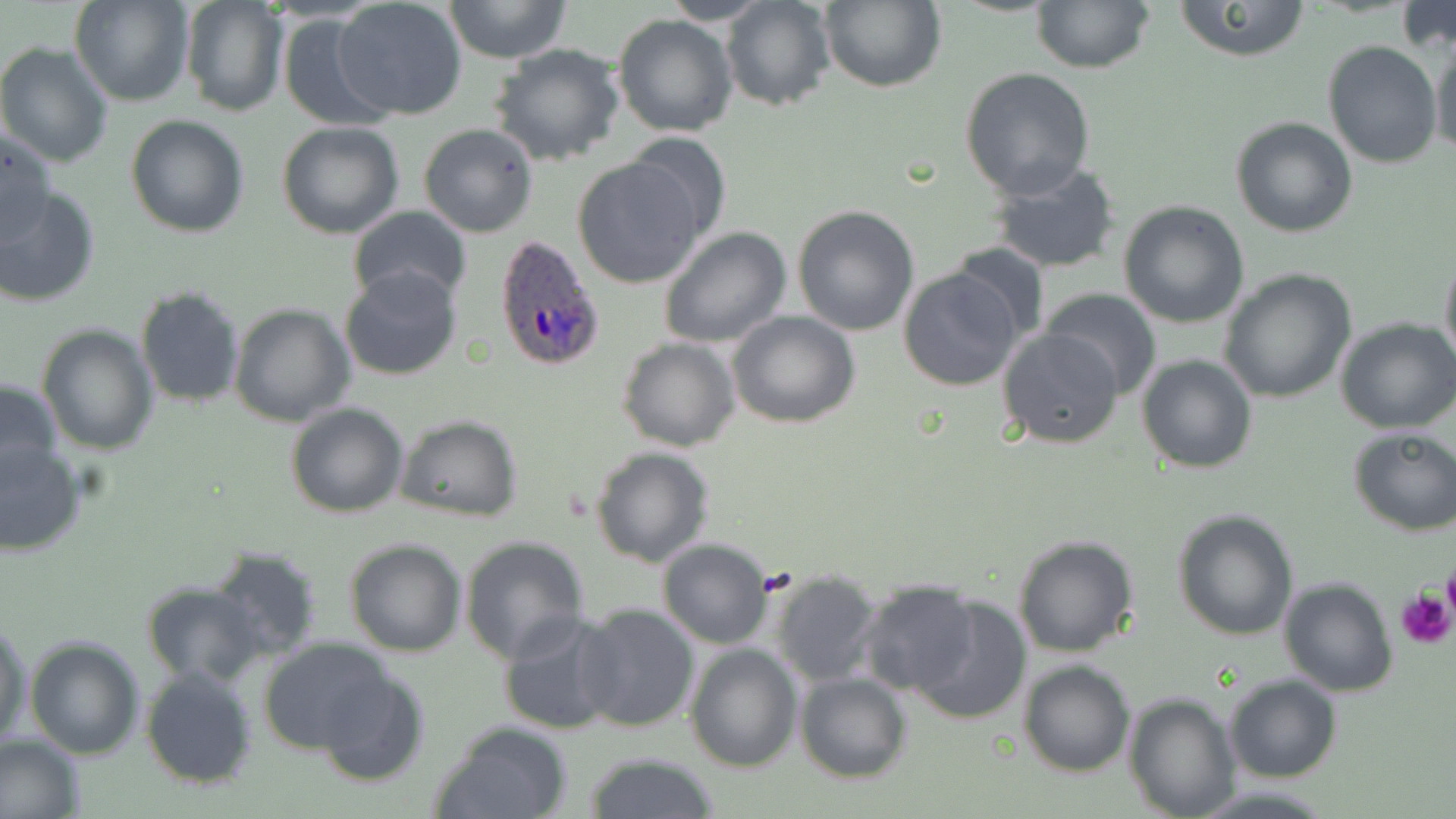
slide-level diagnosis = Plasmodium ovale
modality = optical microscopy
preparation = thin blood smear
uninfected red blood cell locations = approximate bounding boxes as (x1, y1, x2, y2) in pixels: (70, 0, 195, 106), (443, 0, 572, 62), (658, 0, 772, 25), (719, 0, 836, 113), (820, 0, 947, 93), (1172, 0, 1313, 61), (1030, 1, 1155, 72), (179, 2, 288, 117), (332, 2, 468, 122), (1395, 4, 1456, 53), (613, 12, 740, 138), (277, 14, 397, 132), (1428, 36, 1455, 160), (1322, 40, 1442, 169), (0, 42, 117, 169), (489, 43, 628, 168), (959, 65, 1096, 199), (124, 115, 250, 239), (1231, 116, 1359, 238), (277, 122, 404, 239), (419, 122, 540, 239), (2, 125, 55, 247), (620, 131, 733, 244), (572, 156, 708, 289), (987, 160, 1122, 276), (0, 186, 100, 309), (1117, 199, 1250, 328), (792, 203, 922, 336), (347, 205, 473, 310), (658, 226, 791, 349), (947, 240, 1050, 344), (1439, 252, 1456, 375), (340, 266, 461, 381), (897, 266, 1025, 391), (1217, 268, 1357, 404), (135, 284, 246, 409), (1041, 289, 1163, 400), (229, 303, 355, 427), (727, 310, 860, 428), (1334, 317, 1456, 436), (36, 324, 158, 454), (997, 327, 1125, 448), (617, 337, 741, 453), (1136, 353, 1258, 475), (0, 376, 64, 488), (285, 401, 410, 518), (394, 415, 523, 523), (1347, 426, 1456, 535), (0, 438, 88, 556), (589, 446, 714, 568), (1171, 508, 1300, 641), (457, 534, 591, 665), (1012, 534, 1141, 658), (656, 537, 776, 648), (344, 538, 468, 658), (207, 545, 326, 661), (768, 568, 886, 687), (1278, 576, 1396, 696), (855, 579, 982, 698), (139, 581, 266, 689), (911, 597, 1031, 727), (576, 603, 700, 733), (497, 612, 621, 735), (0, 618, 32, 751), (24, 635, 145, 759), (259, 637, 396, 759), (684, 642, 801, 771), (315, 659, 430, 785), (1018, 660, 1135, 777), (140, 665, 258, 788), (795, 673, 913, 784), (1224, 674, 1342, 783), (1123, 692, 1241, 818), (429, 720, 575, 819), (0, 732, 86, 819), (582, 752, 720, 819), (1192, 782, 1336, 818)
field of view = single
magnification = 1000x
Plasmodium ovale-infected red blood cell locations = approximate bounding boxes as (x1, y1, x2, y2) in pixels: (492, 234, 608, 370)
stain = May-Grünwald-Giemsa
image size = 1456×819 pixels
platelet locations = approximate bounding boxes as (x1, y1, x2, y2) in pixels: (1441, 563, 1456, 625), (1396, 590, 1454, 650)